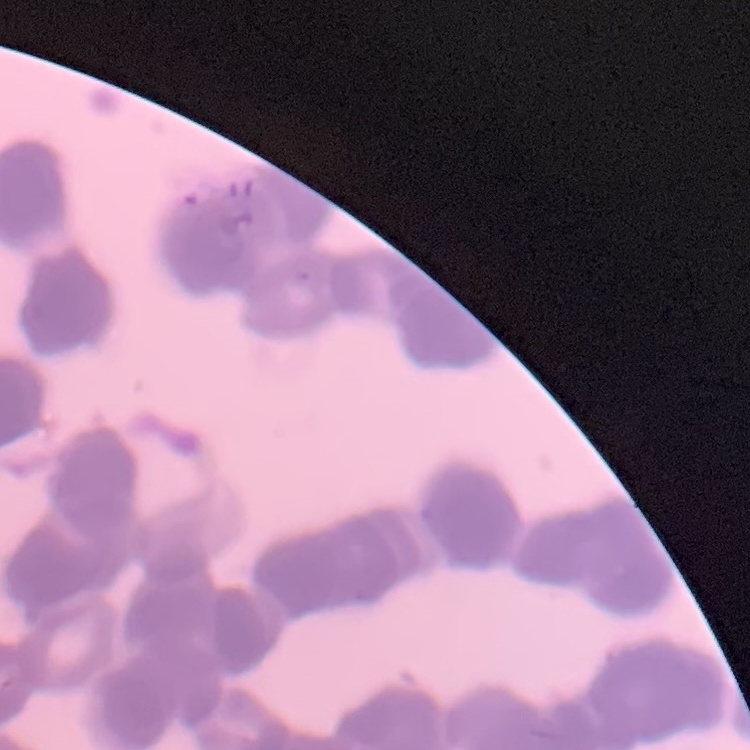
Summary:
  - Erythrocyte morphology: rouleaux formation
  - Stain: Field's or Giemsa
  - Image type: square crop of a larger photomicrograph
  - Preparation: thin blood smear